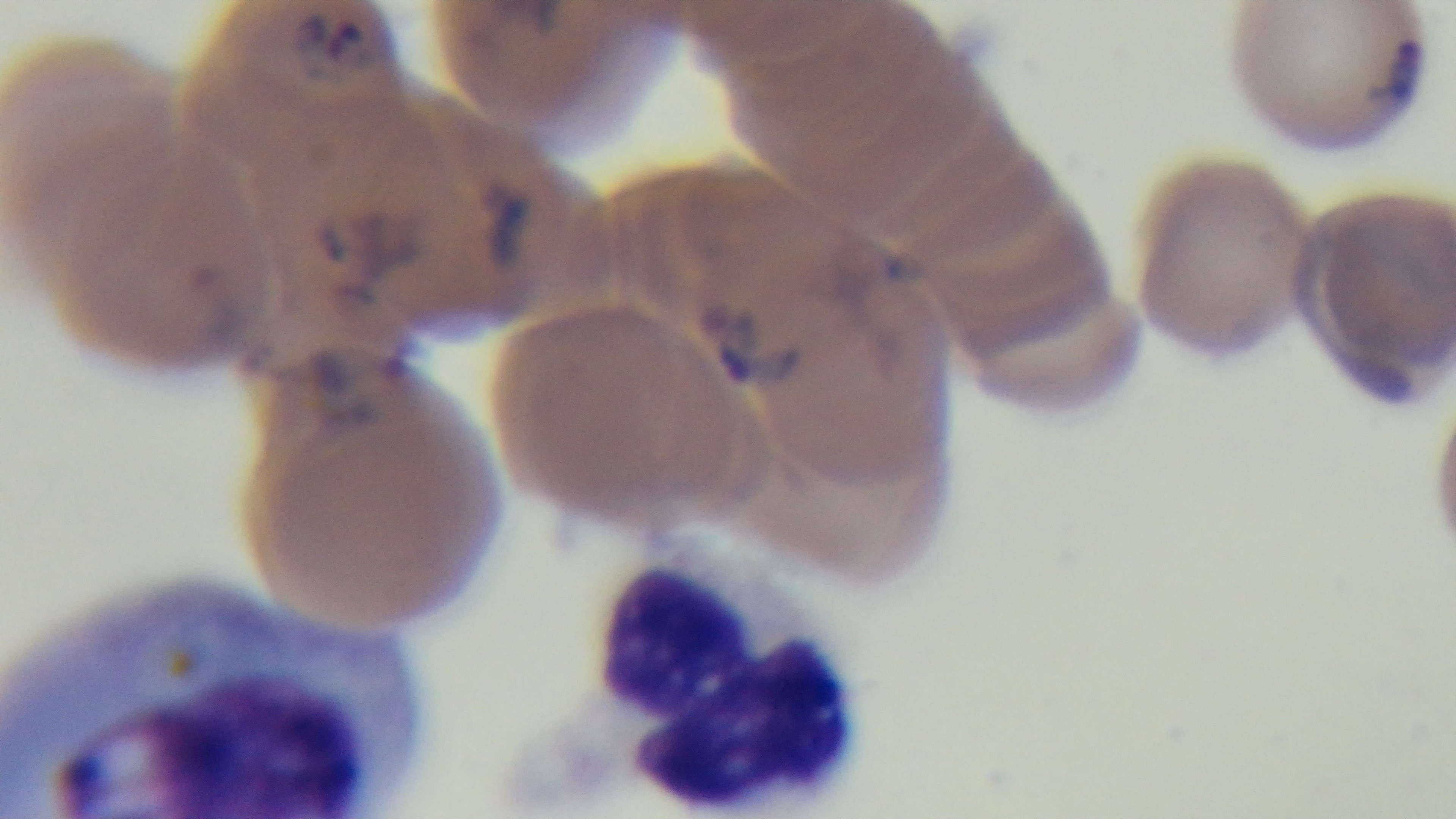

Mounted 4K digital camera. Malaria status: positive. Light microscopy. 100x oil-immersion objective. Giemsa stain. Preparation: thin blood film. One field from the slide.